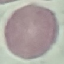
malaria status = uninfected
stain = Giemsa
image type = cell patch, automatically extracted from a larger field of view and resized to 64 × 64 pixels
capture = smartphone camera at the microscope eyepiece
preparation = thin smear